Outline every leukocyte.
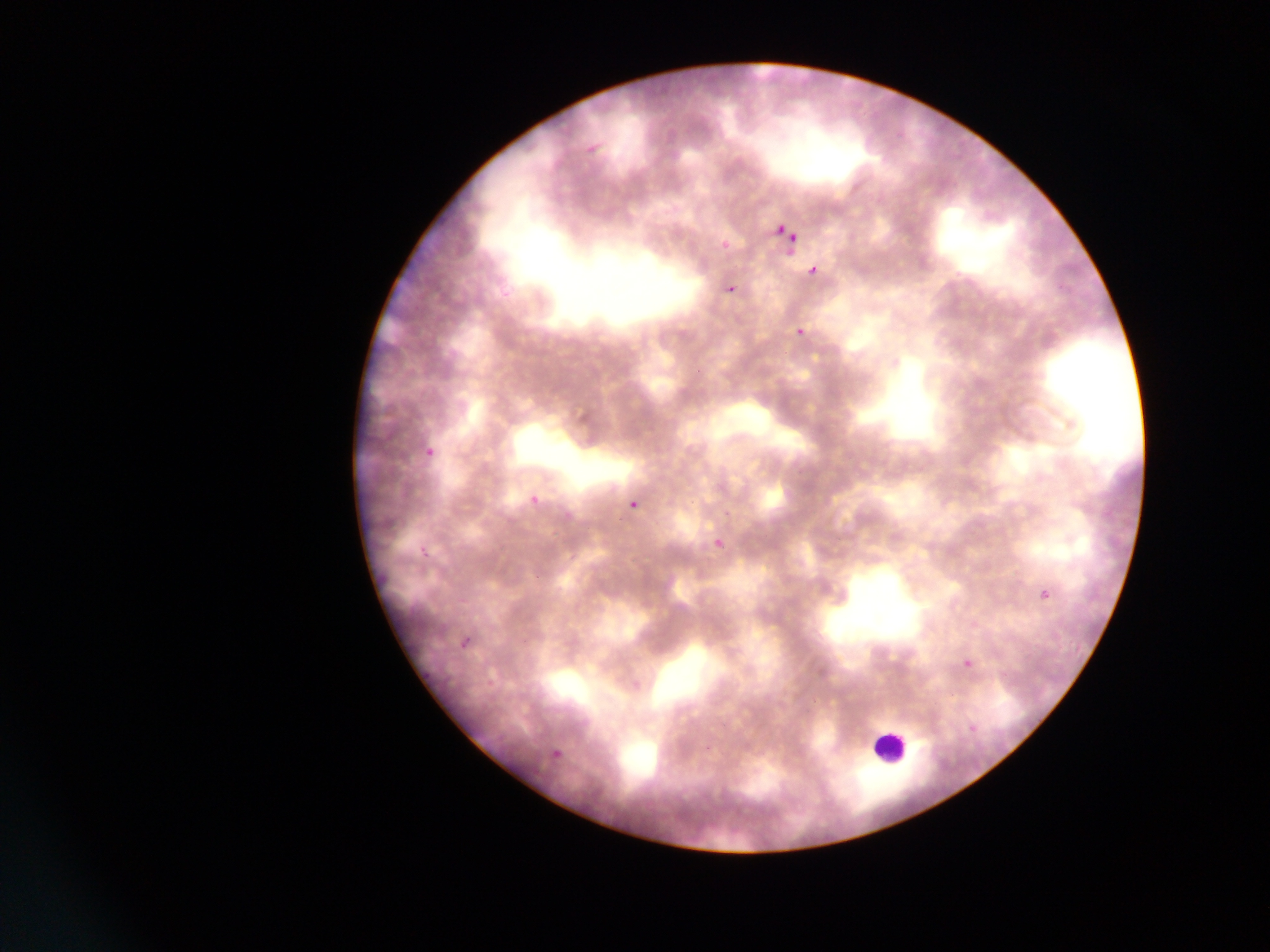

Approximate bounding boxes as {left, top, right, bottom} in pixels.
Leukocytes: {868, 728, 915, 772}.

Plasmodium parasite locations: {771, 222, 794, 242}, {778, 224, 803, 249}, {715, 233, 736, 257}, {807, 263, 823, 279}, {722, 279, 744, 302}, {791, 323, 813, 346}, {421, 441, 437, 457}, {523, 491, 539, 504}, {627, 500, 640, 511}, {707, 528, 738, 560}, {416, 533, 428, 557}, {1035, 581, 1057, 608}, {458, 622, 479, 653}, {959, 653, 979, 675}, {417, 667, 431, 679}, {961, 722, 979, 738}, {547, 743, 569, 766}. Single field of view. Thin blood film. Image is 1270×952 pixels. Sample from Ghana. Mobile-phone photograph taken through the microscope.